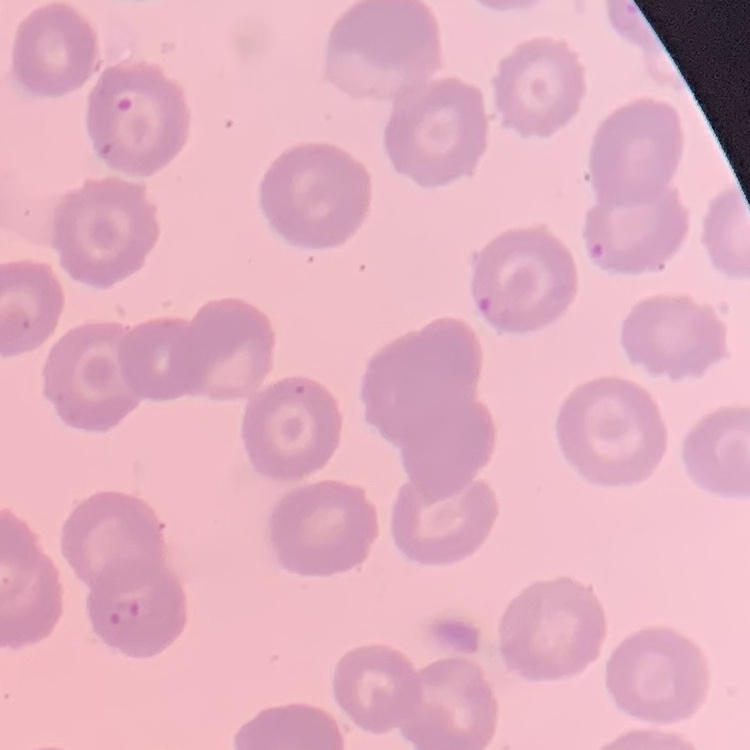
The red blood cells show no rouleaux formation. Thin blood smear. Field's or Giemsa stain. Square crop of a larger photomicrograph.